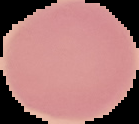
{
  "image_type": "cell region segmented out of the field of view; surrounding area masked to black",
  "image_size": "139×124 pixels",
  "preparation": "thin blood smear",
  "malaria_status": "uninfected"
}